Evaluate for Plasmodium parasites.
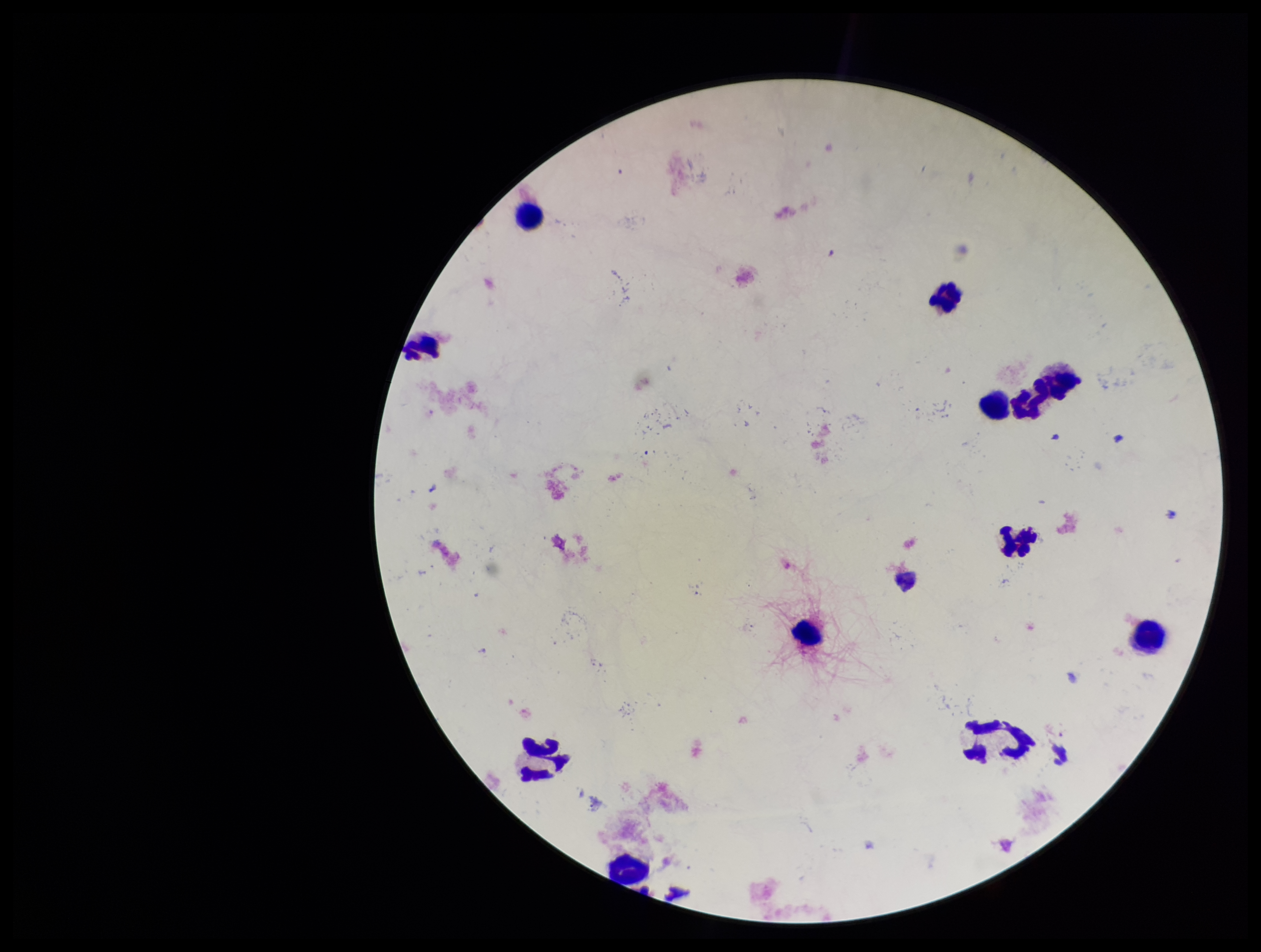
None seen.

Summary:
  - Parasite count: 0
  - Preparation: thick blood smear
  - Patient malaria status: negative
  - Stain: Giemsa
  - Field of view: single
  - Leukocyte count: 10
  - Image size: 1261×952 pixels
  - Capture: smartphone photograph through the microscope eyepiece